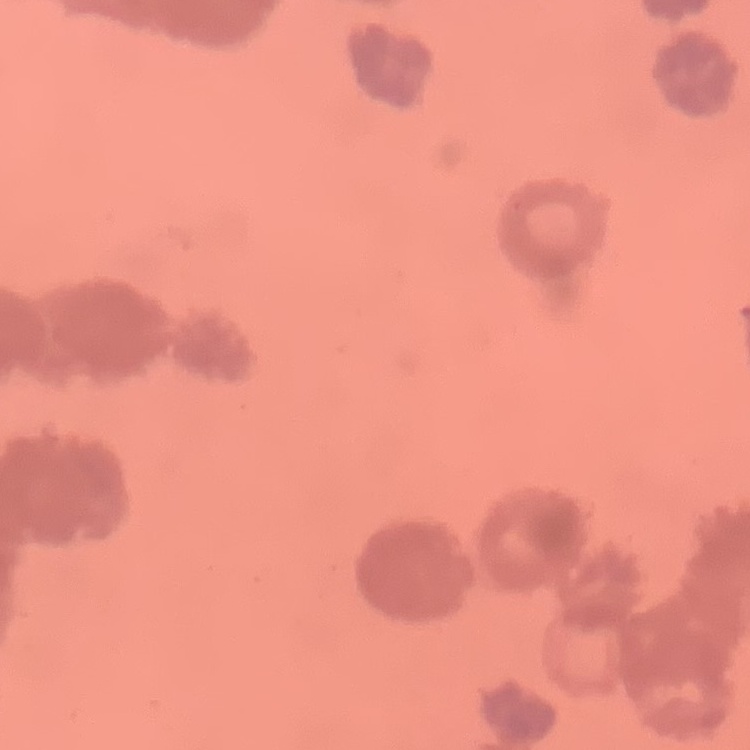

Summary:
  - Red blood cell morphology: rouleaux formation
  - Preparation: thin blood smear
  - Stain: Field's or Giemsa
  - Image type: one tile cut from a larger photomicrograph